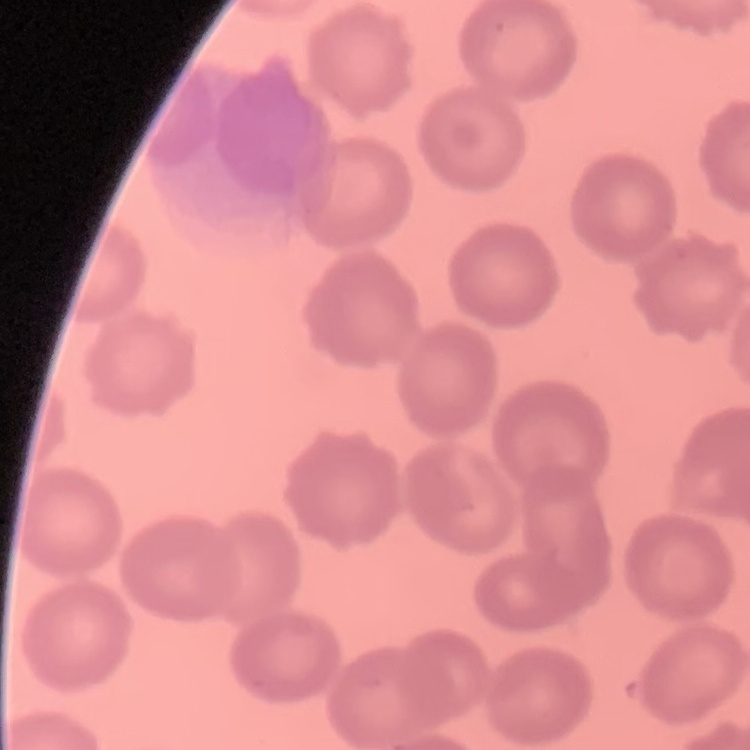

The erythrocytes show no rouleaux formation. Field's or Giemsa stain. One tile cut from a larger photomicrograph. Thin blood smear.